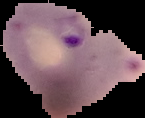
image type = segmented cell region with the area outside set to black
image size = 145×118 pixels
preparation = thin blood film
result = Plasmodium parasites identified